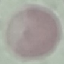
malaria status = uninfected
preparation = thin blood smear
image type = cell patch, automatically extracted from a larger field of view and resized to 64 × 64 pixels
capture = smartphone through the microscope eyepiece
stain = Giemsa